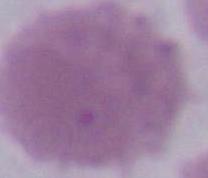

magnification = 1000x
identification = red blood cell
modality = photomicrograph